Outline each blood parasite and name the species.
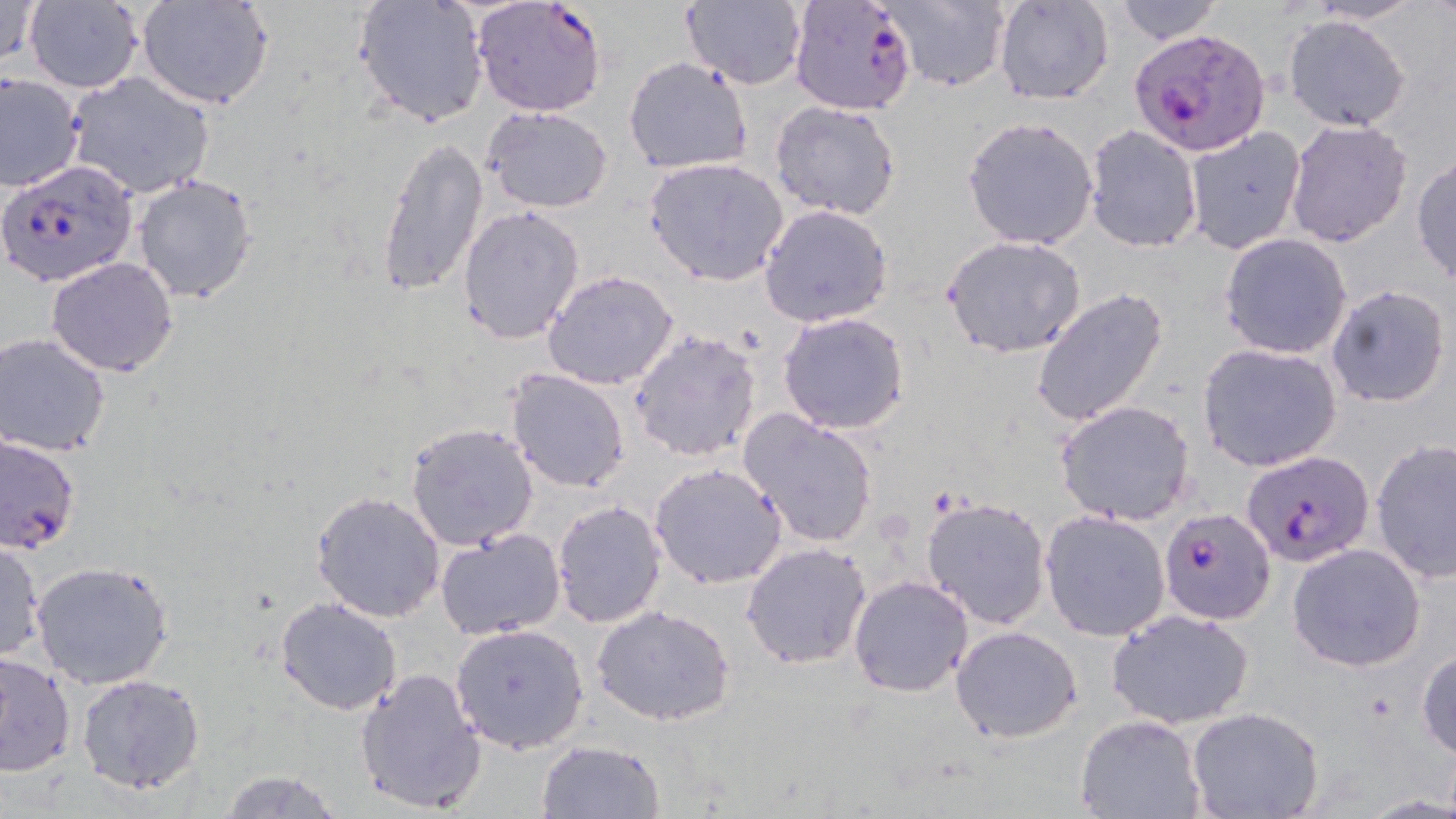
Approximate bounding boxes as [x1, y1, x2, y2] in pixels.
Plasmodium falciparum-infected red blood cells: [471, 0, 607, 117], [788, 0, 920, 116], [1130, 25, 1269, 156], [2, 157, 137, 286], [0, 435, 80, 555], [1247, 445, 1378, 563], [1163, 511, 1279, 630].
No Plasmodium ovale, Plasmodium malariae, Plasmodium vivax, Babesia divergens, or Trypanosoma brucei observed.

Summary:
  - Uninfected red blood cell locations: [0, 0, 41, 68], [354, 0, 489, 128], [876, 0, 1012, 92], [992, 0, 1114, 106], [1301, 0, 1430, 24], [23, 1, 144, 91], [136, 1, 273, 110], [679, 1, 809, 88], [1114, 1, 1225, 44], [1282, 13, 1412, 133], [624, 55, 753, 175], [1, 72, 82, 192], [64, 72, 213, 199], [769, 101, 902, 221], [482, 104, 614, 214], [962, 115, 1099, 251], [1285, 118, 1413, 249], [1182, 125, 1305, 254], [1083, 126, 1203, 252], [376, 137, 488, 298], [1411, 153, 1456, 287], [644, 157, 789, 285], [132, 173, 258, 303], [758, 204, 893, 328], [457, 205, 584, 344], [1218, 232, 1352, 358], [941, 235, 1087, 358], [45, 256, 179, 378], [542, 269, 679, 391], [1325, 284, 1452, 408], [1031, 288, 1169, 429], [777, 311, 911, 434], [630, 327, 762, 464], [0, 332, 111, 457], [1197, 341, 1342, 471], [504, 369, 631, 493], [1055, 400, 1195, 526], [736, 408, 880, 548], [406, 422, 538, 552], [1371, 438, 1456, 584], [649, 462, 786, 589], [311, 492, 446, 621], [920, 495, 1053, 631], [552, 500, 666, 629], [1040, 510, 1171, 642], [435, 527, 566, 640], [0, 539, 45, 662], [741, 543, 872, 668], [1286, 543, 1427, 671], [30, 560, 175, 689], [847, 574, 974, 699], [275, 597, 401, 715], [591, 606, 737, 728], [1106, 608, 1255, 730], [450, 623, 589, 753], [950, 626, 1082, 743], [1416, 646, 1456, 761], [0, 652, 75, 776], [355, 667, 487, 813], [75, 674, 205, 795], [1187, 707, 1324, 819], [1075, 713, 1205, 818], [537, 740, 663, 819], [213, 768, 345, 817]
  - Slide-level diagnosis: Plasmodium falciparum
  - Image size: 1456×819 pixels
  - Field of view: single
  - Modality: optical microscopy
  - Stain: May-Grünwald-Giemsa
  - Preparation: thin blood film
  - Magnification: 1000x